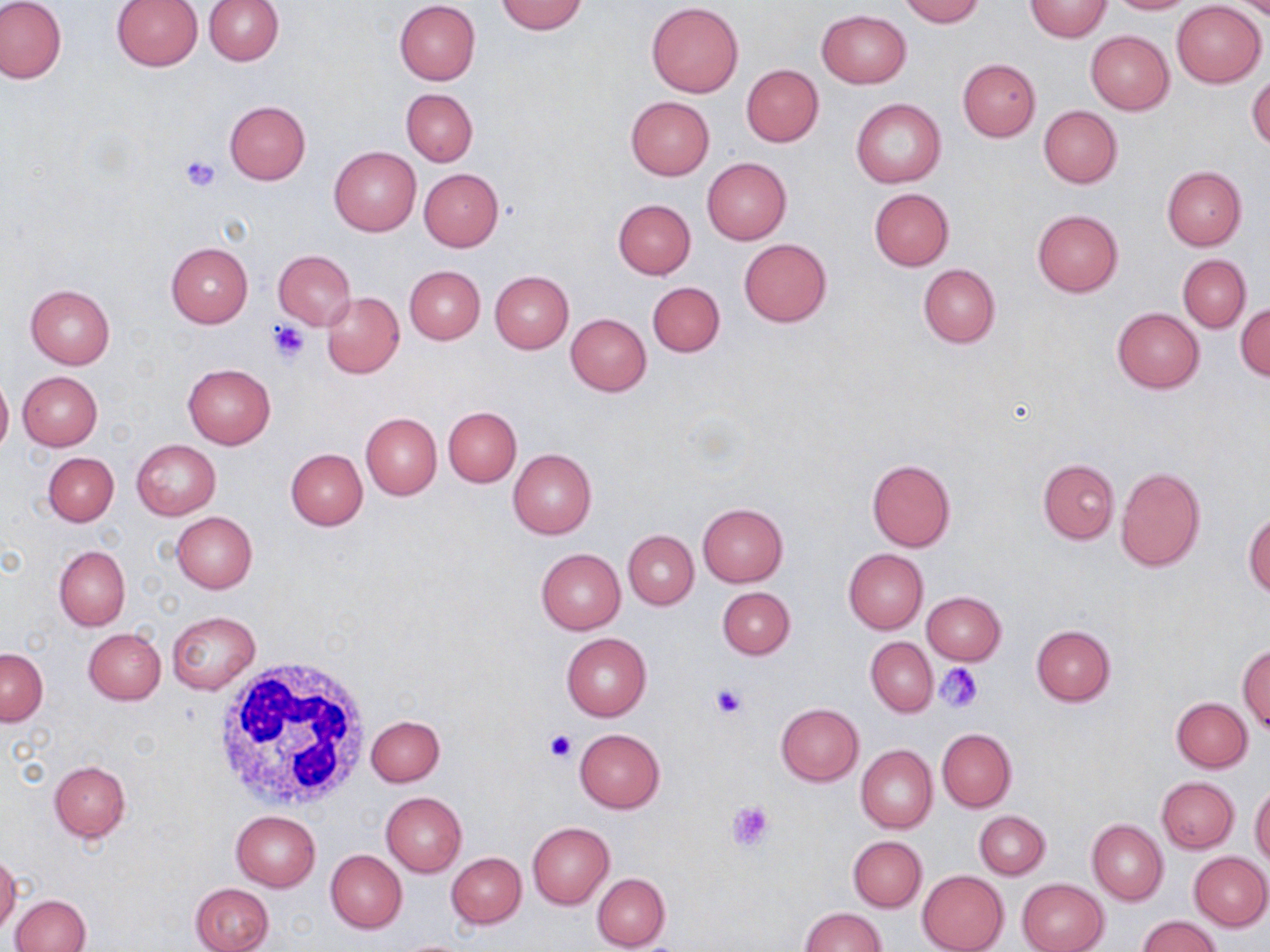

Approximate bounding boxes as (x1, y1, x2, y2) in pixels. White blood cell locations: (210, 654, 375, 815). Platelet locations: (180, 155, 222, 192), (268, 320, 309, 362), (936, 663, 984, 712), (710, 682, 745, 718), (543, 730, 576, 762), (727, 798, 777, 850). Uninfected red blood cell locations: (0, 0, 66, 84), (204, 0, 284, 65), (898, 0, 984, 25), (1026, 0, 1111, 41), (1105, 0, 1195, 14), (110, 1, 202, 71), (394, 1, 481, 85), (495, 1, 587, 35), (1172, 1, 1266, 87), (646, 2, 743, 97), (816, 10, 911, 89), (1085, 31, 1174, 115), (957, 58, 1041, 140), (741, 64, 824, 147), (1247, 73, 1270, 151), (401, 88, 477, 166), (625, 96, 714, 179), (851, 99, 946, 188), (224, 100, 311, 184), (1039, 106, 1123, 188), (330, 146, 422, 235), (702, 158, 792, 245), (1162, 166, 1246, 249), (418, 168, 504, 251), (868, 188, 955, 270), (614, 199, 696, 279), (1032, 209, 1123, 296), (738, 238, 832, 327), (166, 242, 253, 327), (273, 249, 356, 330), (1178, 254, 1250, 332), (918, 263, 1000, 348), (404, 266, 485, 344), (489, 271, 574, 353), (647, 281, 725, 356), (25, 283, 116, 368), (322, 292, 404, 378), (1235, 302, 1270, 380), (1112, 307, 1204, 392), (566, 312, 651, 395), (182, 363, 276, 448), (0, 370, 12, 457), (18, 371, 102, 450), (443, 406, 521, 486), (361, 412, 442, 500), (131, 439, 221, 518), (286, 448, 368, 530), (508, 448, 597, 538), (43, 452, 119, 526), (866, 459, 956, 551), (1037, 459, 1119, 544), (1116, 466, 1206, 572), (698, 503, 788, 586), (1244, 510, 1270, 597), (172, 512, 257, 593), (623, 530, 698, 609), (54, 546, 130, 631), (536, 548, 625, 634), (843, 549, 928, 634), (718, 587, 794, 659), (921, 591, 1006, 665), (166, 611, 259, 693), (1031, 624, 1116, 705), (83, 628, 166, 705), (562, 632, 652, 721), (865, 637, 937, 717), (1238, 644, 1270, 731), (0, 649, 48, 726), (1171, 697, 1252, 772), (776, 703, 864, 786), (367, 714, 444, 787), (937, 727, 1017, 812), (575, 729, 665, 813), (856, 745, 937, 833), (49, 760, 131, 842), (1156, 776, 1239, 853), (1250, 784, 1270, 867), (381, 792, 467, 877), (230, 810, 321, 891), (974, 812, 1050, 879), (1087, 819, 1167, 904), (528, 822, 614, 909), (848, 836, 926, 912), (326, 849, 407, 932), (447, 852, 526, 928), (1189, 852, 1270, 930), (0, 854, 21, 935), (917, 869, 1009, 952), (592, 872, 671, 951), (1017, 878, 1109, 952), (190, 883, 273, 951), (10, 894, 90, 951), (799, 907, 888, 952), (1137, 916, 1222, 952). Slide-level diagnosis: no evidence of blood parasites. May-Grünwald-Giemsa stain. Light microscopy. Single field of view. Image is 1270×952 pixels. Thin blood film. 1000x magnification.